Classify this cell by malaria status.
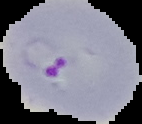
Parasitized.

{
  "image_size": "142×124 pixels",
  "image_type": "segmented cell region on a black background",
  "preparation": "thin blood film"
}